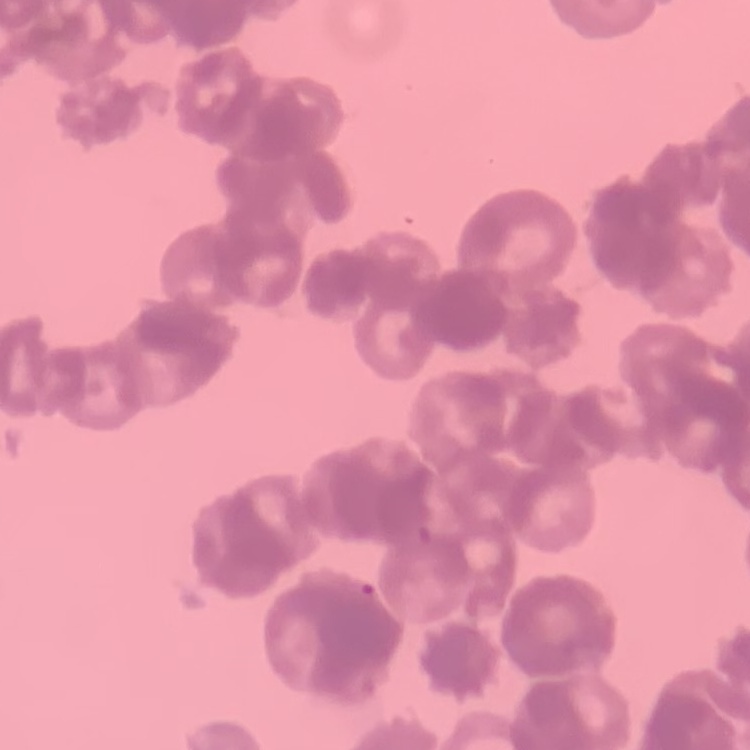
Summary:
  - Red blood cell morphology: rouleaux formation
  - Image type: square crop of a larger photomicrograph
  - Preparation: thin blood smear
  - Stain: Field's or Giemsa